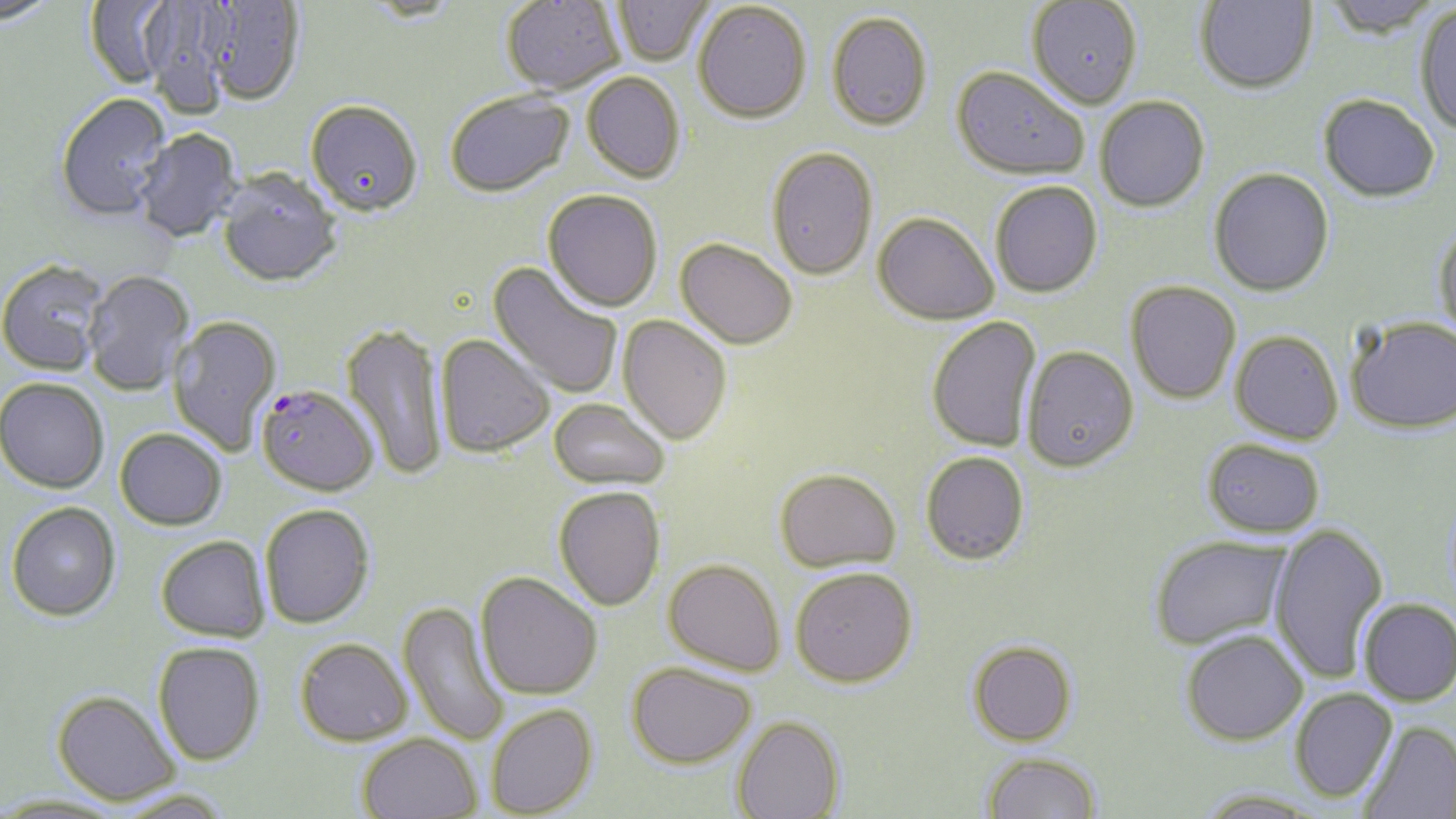
Approximate bounding boxes as [x1, y1, x2, y2] in pixels. Plasmodium falciparum-infected red blood cell locations: [256, 384, 378, 496]. Uninfected red blood cell locations: [501, 0, 624, 96], [612, 0, 713, 67], [1027, 0, 1141, 109], [1321, 0, 1444, 38], [85, 1, 177, 91], [1195, 1, 1317, 94], [201, 2, 306, 107], [693, 2, 811, 123], [143, 3, 231, 119], [1414, 4, 1456, 137], [826, 11, 933, 130], [951, 66, 1090, 181], [582, 72, 686, 183], [445, 90, 575, 199], [1318, 94, 1440, 202], [55, 95, 173, 223], [1095, 96, 1210, 212], [305, 101, 424, 220], [135, 129, 243, 244], [766, 146, 878, 280], [1208, 167, 1334, 296], [217, 171, 342, 289], [989, 181, 1102, 297], [542, 190, 662, 312], [873, 212, 999, 324], [1432, 221, 1456, 341], [675, 238, 798, 349], [0, 261, 109, 377], [487, 261, 624, 401], [83, 271, 194, 396], [1125, 280, 1242, 404], [168, 315, 282, 456], [618, 315, 732, 445], [1345, 315, 1456, 434], [926, 317, 1043, 452], [341, 321, 449, 482], [1230, 331, 1343, 444], [436, 334, 555, 458], [1022, 346, 1138, 472], [0, 378, 110, 494], [549, 398, 670, 490], [115, 428, 227, 530], [1202, 439, 1326, 536], [920, 451, 1029, 565], [774, 467, 901, 572], [553, 486, 666, 610], [6, 502, 121, 621], [259, 504, 374, 628], [1269, 522, 1388, 683], [156, 535, 271, 642], [1149, 535, 1293, 651], [663, 558, 785, 676], [790, 567, 917, 687], [476, 572, 603, 699], [1358, 598, 1456, 705], [397, 600, 511, 746], [1180, 629, 1308, 745], [294, 638, 412, 745], [967, 639, 1079, 746], [153, 642, 265, 765], [626, 662, 757, 767], [1290, 689, 1397, 802], [51, 690, 181, 806], [485, 704, 598, 817], [731, 715, 846, 819], [1358, 721, 1456, 819], [356, 733, 482, 819], [980, 751, 1103, 818], [110, 791, 236, 819], [0, 795, 125, 819]. Slide-level diagnosis: Plasmodium falciparum. Optical microscopy. Image is 1456×819 pixels. Thin blood film. May-Grünwald-Giemsa stain. 1000x magnification. Single field of view.